Locate every Plasmodium parasite and every leukocyte.
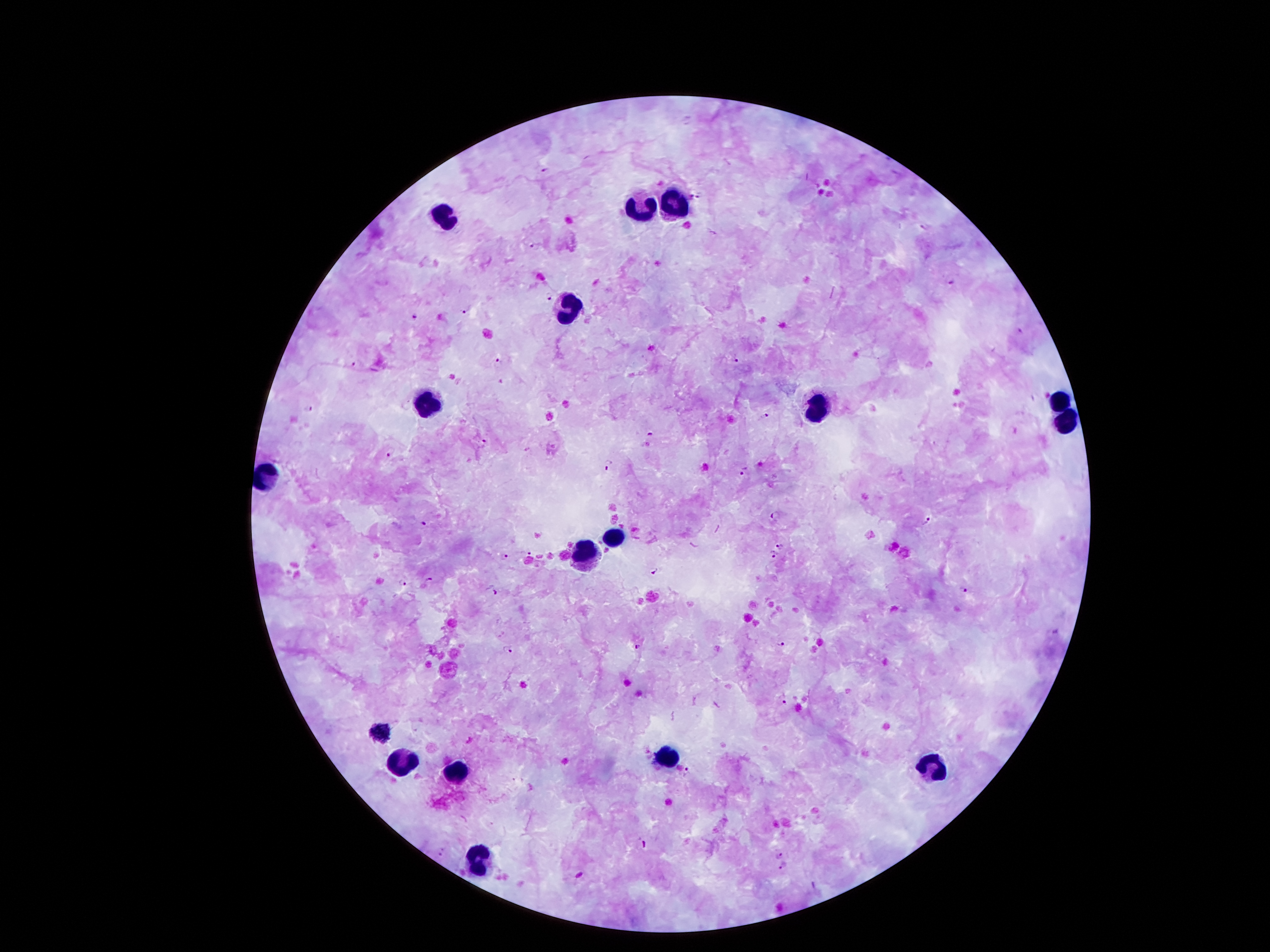
Approximate centers as {x, y} in pixels.
Plasmodium parasites: {545, 169}, {698, 194}, {534, 245}, {951, 283}, {548, 297}, {465, 307}, {415, 316}, {1020, 329}, {737, 358}, {356, 360}, {497, 361}, {308, 409}, {767, 414}, {652, 434}, {482, 442}, {390, 454}, {610, 465}, {746, 472}, {774, 514}, {929, 519}, {425, 523}, {781, 545}, {528, 553}, {775, 556}, {504, 557}, {655, 570}, {431, 579}, {402, 584}, {962, 591}, {495, 592}, {779, 643}, {508, 648}, {638, 650}, {783, 698}, {685, 771}, {643, 843}, {441, 850}, {779, 857}, {781, 867}, {580, 874}.
Leukocytes: {678, 199}, {641, 204}, {445, 218}, {569, 311}, {1059, 395}, {426, 403}, {812, 412}, {1062, 426}, {266, 479}, {613, 538}, {588, 560}, {381, 733}, {667, 759}, {927, 764}, {398, 767}, {454, 770}, {479, 859}.

100x magnification. Image is 1270×952 pixels. Smartphone photograph taken through the microscope eyepiece. Single field of view. Giemsa stain. Thick blood smear. Patient malaria status: infected with Plasmodium falciparum.